Evaluate for malaria.
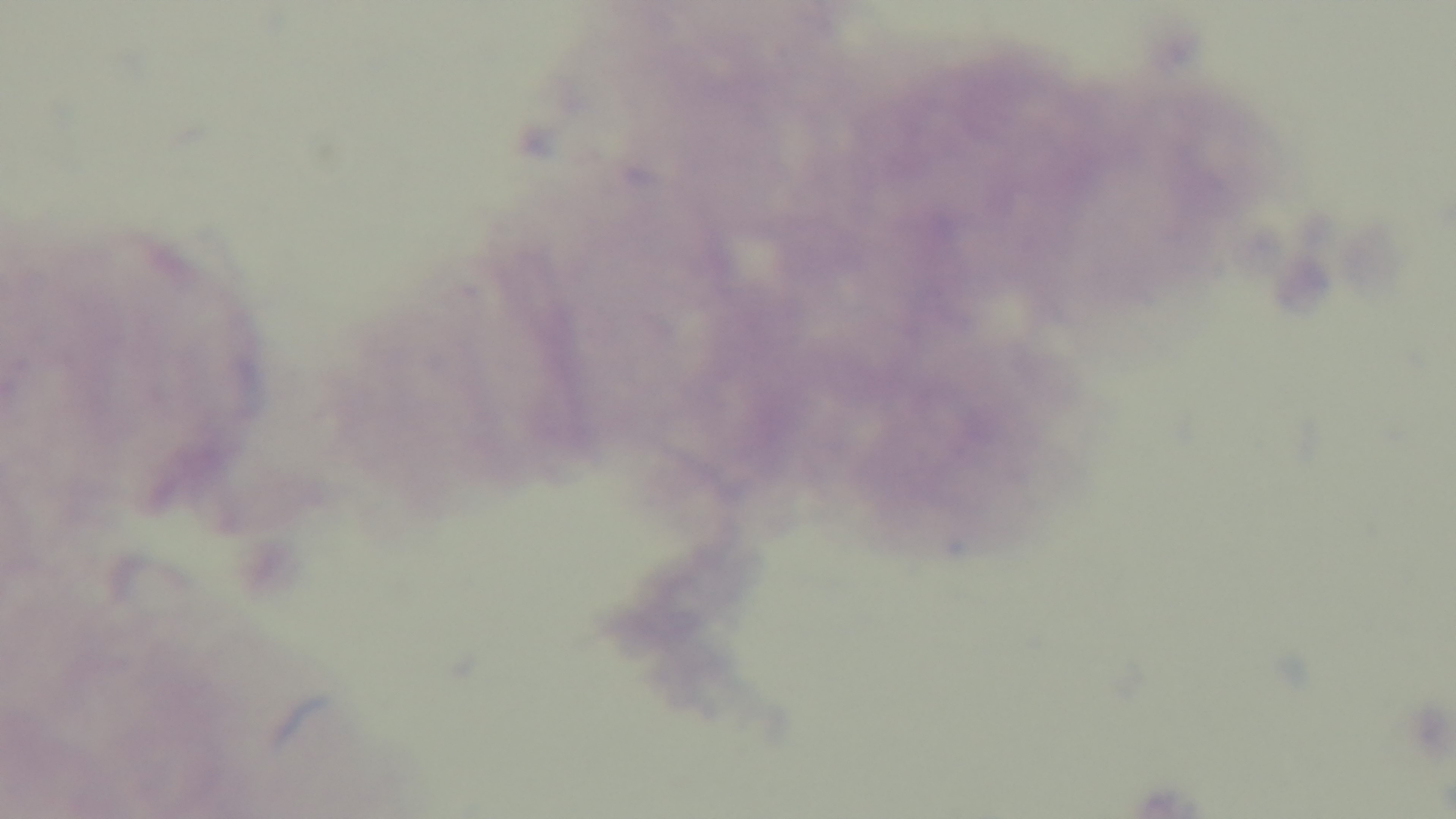
Negative.

objective = 100x oil immersion
preparation = thick smear
field of view = single
capture = mounted 4K digital camera
stain = Giemsa
modality = light microscopy